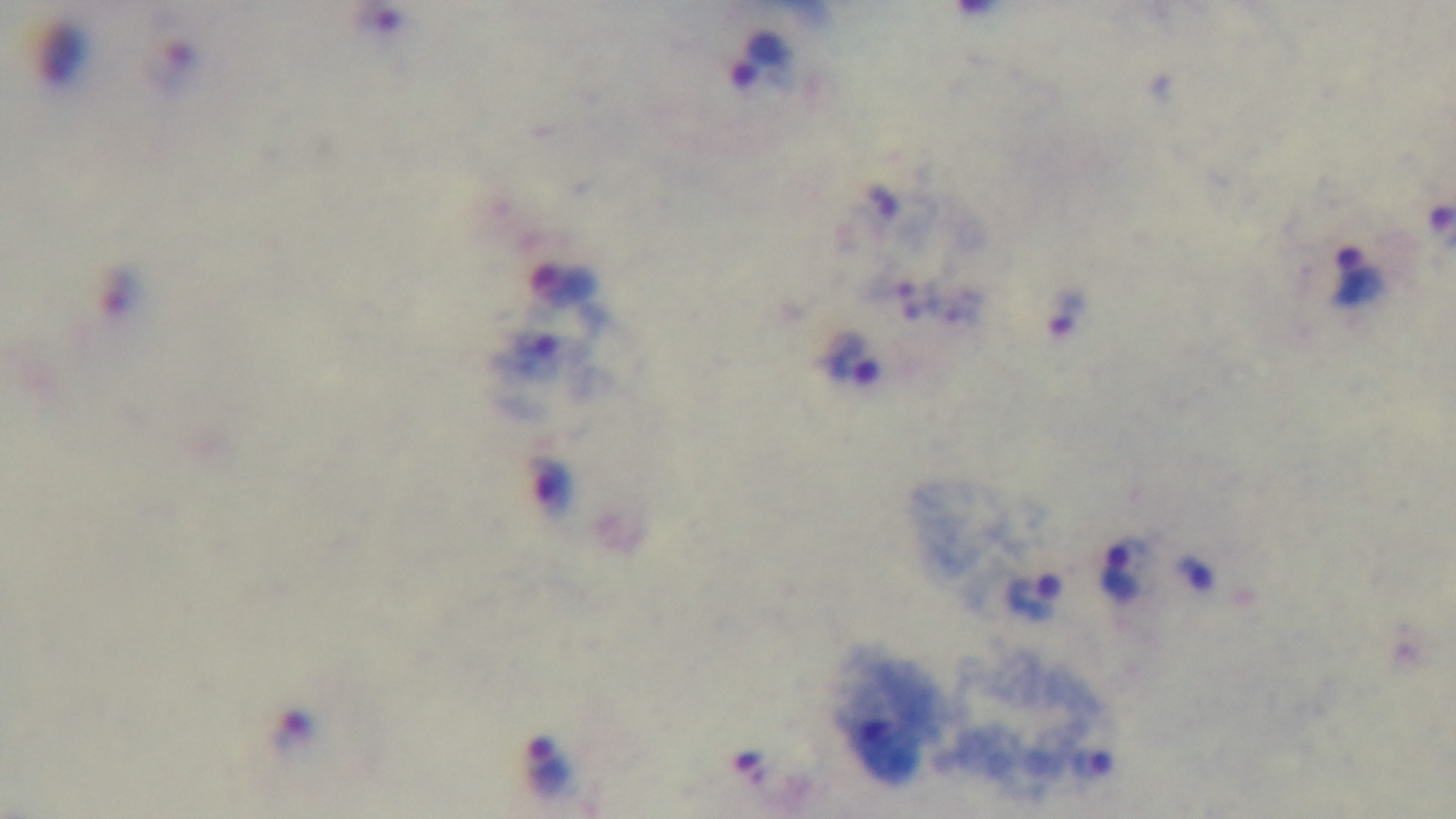

stain = Giemsa
objective = 100x oil immersion
modality = light microscopy
capture = mounted 4K digital camera
preparation = thick
malaria status = infected
field of view = one from the slide